Comment on the morphology of the erythrocytes.
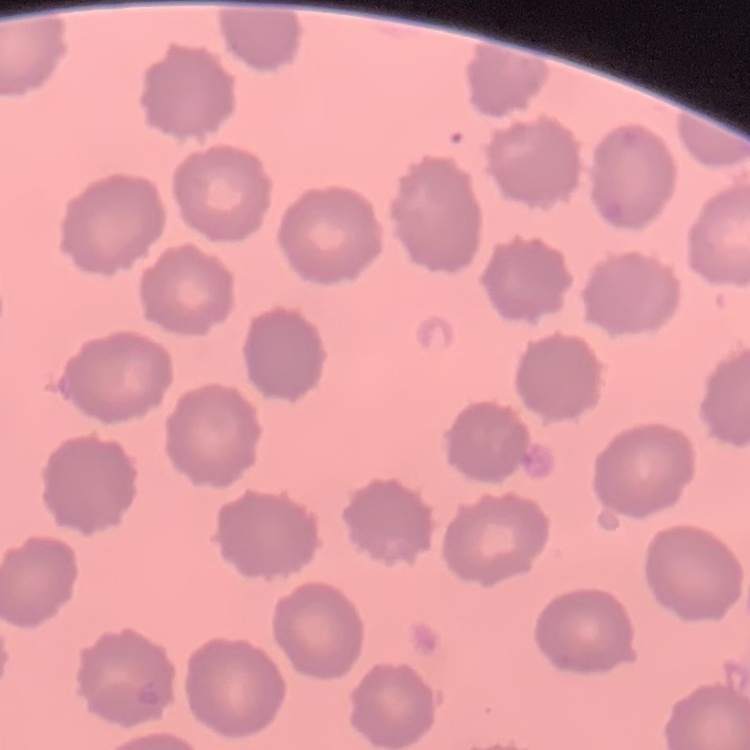
No rouleaux formation.

Summary:
  - Stain: Field's or Giemsa
  - Preparation: thin blood film
  - Image type: square crop of a larger photomicrograph